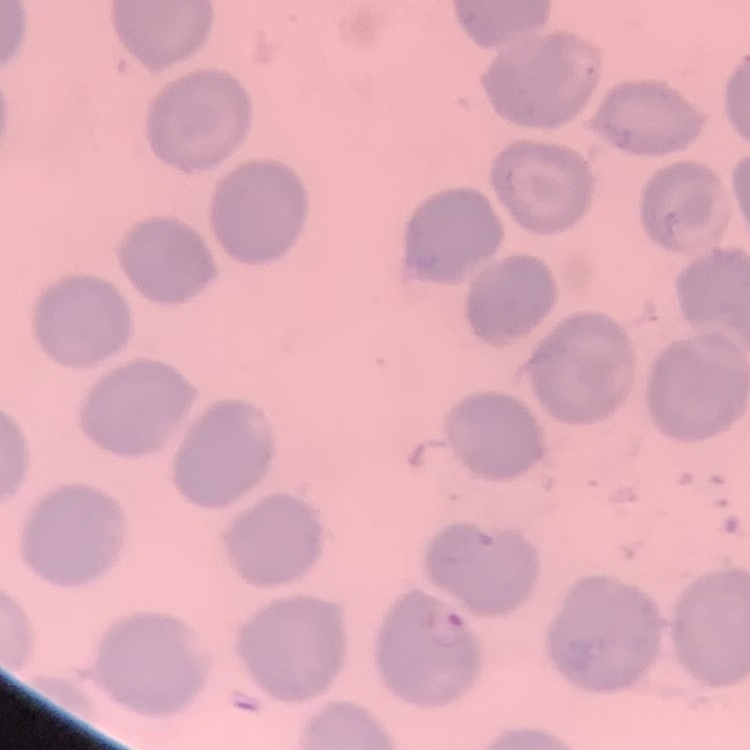

erythrocyte morphology = no rouleaux formation
image type = square crop of a larger photomicrograph
stain = Field's or Giemsa
preparation = thin blood film